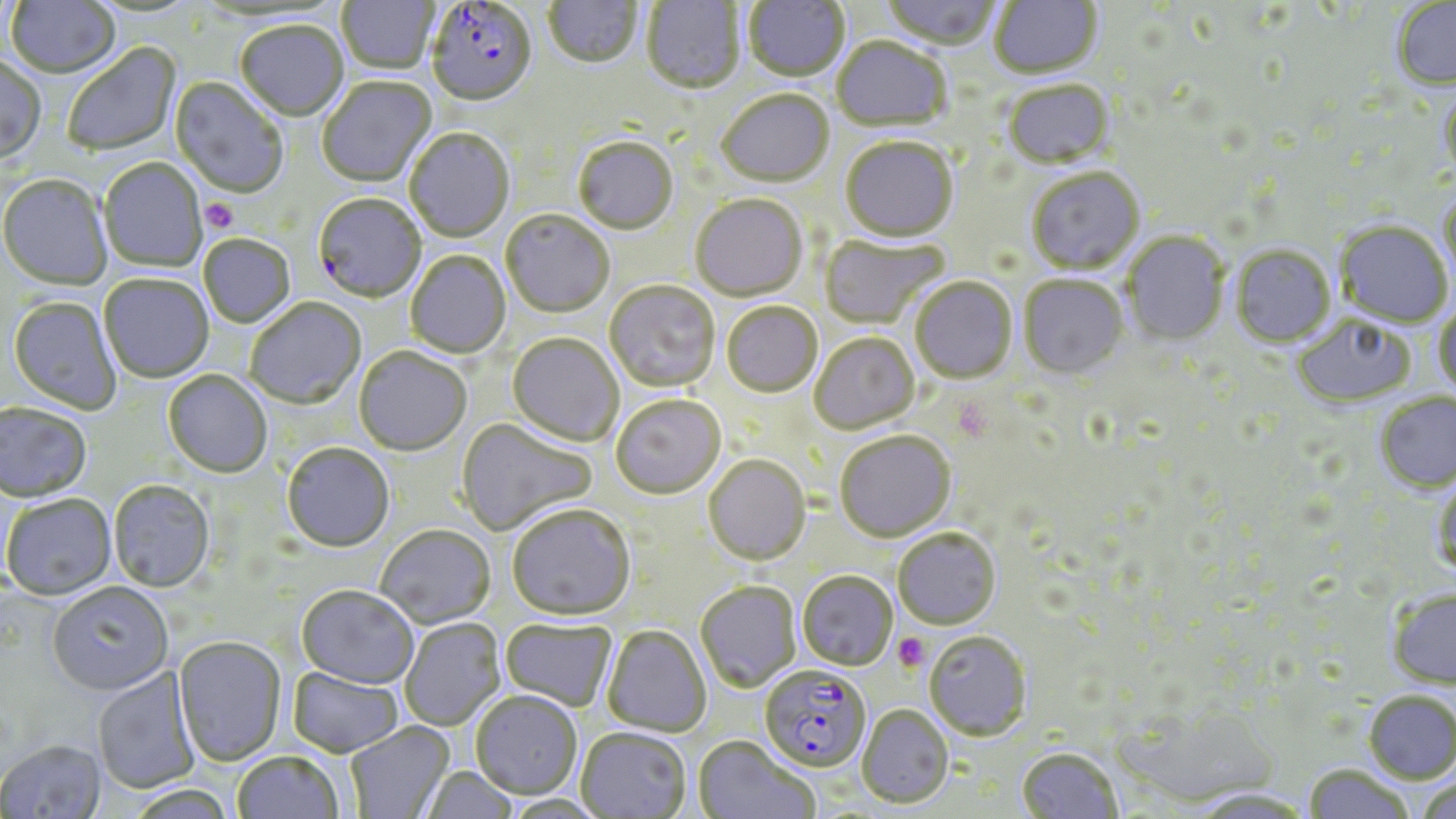
Approximate bounding boxes as [x1, y1, x2, y2] in pixels. Platelet locations: [200, 199, 238, 233], [894, 633, 930, 670]. Uninfected red blood cell locations: [4, 0, 122, 80], [337, 0, 439, 75], [543, 0, 643, 71], [743, 0, 850, 83], [881, 0, 1001, 53], [990, 0, 1102, 81], [641, 1, 746, 96], [1393, 1, 1456, 91], [236, 22, 349, 124], [831, 37, 951, 134], [62, 43, 182, 157], [0, 56, 47, 166], [317, 77, 438, 189], [170, 78, 288, 200], [1004, 82, 1115, 172], [1439, 88, 1456, 179], [717, 91, 834, 189], [405, 129, 515, 244], [573, 139, 678, 236], [841, 139, 958, 243], [98, 159, 207, 273], [1027, 169, 1146, 276], [0, 176, 112, 292], [1439, 188, 1456, 288], [690, 194, 808, 302], [501, 211, 614, 318], [1335, 222, 1453, 328], [1123, 232, 1229, 346], [820, 233, 950, 329], [199, 235, 296, 328], [1231, 246, 1336, 348], [406, 251, 511, 360], [99, 275, 214, 383], [1019, 275, 1128, 380], [910, 277, 1017, 384], [605, 280, 720, 392], [7, 298, 121, 415], [245, 299, 366, 410], [721, 302, 822, 398], [1434, 303, 1456, 397], [1292, 315, 1416, 408], [809, 332, 920, 434], [507, 333, 624, 447], [354, 347, 471, 456], [162, 371, 272, 479], [1375, 392, 1456, 495], [610, 394, 726, 498], [0, 404, 92, 504], [455, 416, 597, 536], [834, 430, 956, 541], [281, 444, 395, 553], [703, 454, 810, 564], [1431, 475, 1456, 579], [108, 481, 215, 593], [2, 495, 117, 601], [507, 503, 635, 620], [374, 525, 496, 629], [893, 528, 1001, 629], [797, 571, 897, 670], [695, 580, 800, 691], [48, 584, 173, 696], [296, 586, 419, 690], [1387, 589, 1456, 689], [400, 618, 506, 732], [500, 619, 617, 711], [602, 625, 711, 737], [925, 630, 1031, 740], [172, 637, 287, 766], [92, 666, 201, 794], [288, 666, 404, 758], [1363, 690, 1456, 785], [471, 691, 583, 799], [858, 704, 954, 807], [345, 722, 454, 818], [575, 727, 691, 818], [694, 736, 819, 819], [0, 740, 107, 818], [1016, 747, 1122, 819], [231, 750, 345, 819], [1304, 764, 1413, 819], [419, 766, 519, 819], [1416, 780, 1456, 819], [122, 785, 238, 818], [1189, 789, 1313, 818]. Plasmodium falciparum-infected red blood cell locations: [425, 1, 537, 109], [313, 195, 426, 304], [760, 665, 871, 772]. Slide-level diagnosis: Plasmodium falciparum. May-Grünwald-Giemsa stain. Thin blood smear. Light microscopy. 1000x magnification. Image is 1456×819 pixels. Single field of view.